Outline each Plasmodium falciparum parasite and classify it by life-cycle stage.
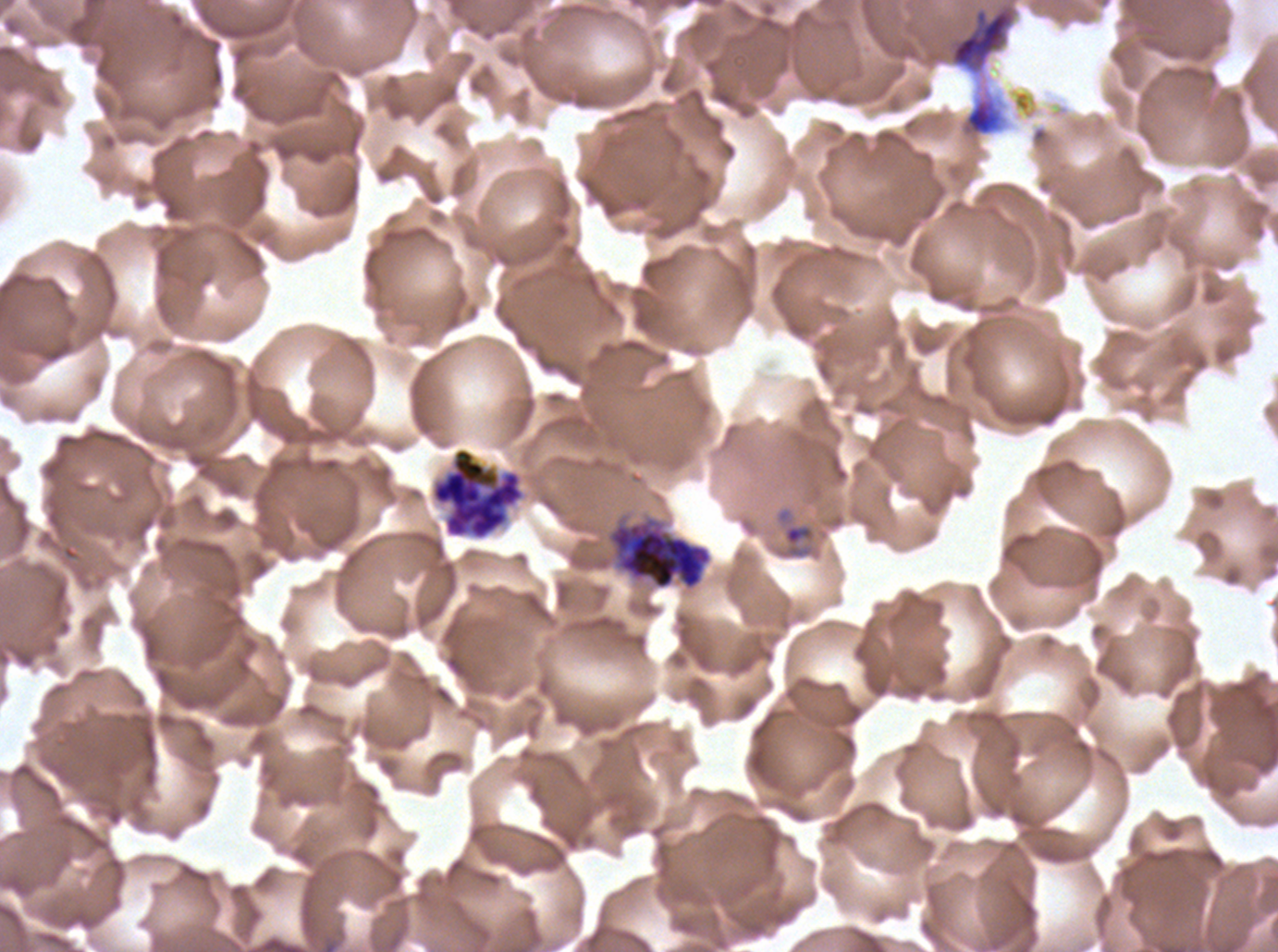
Approximate bounding boxes as [x1, y1, x2, y2] in pixels.
Rings: [775, 507, 817, 560].
Early schizonts: [608, 519, 712, 591].
Segmenters: [429, 446, 527, 542].
No late-ring/early-trophozoite forms, mid trophozoites, late trophozoites, late schizonts, or gametocytes observed.

debris locations = [944, 0, 1019, 76]
life-cycle stages observed = ring, early schizont, segmenter
image size = 1278×952 pixels
field of view = sub-image separated from a larger composite
preparation = thin blood smear
stain = Giemsa
specimen = Plasmodium falciparum from a patient in The Gambia, cultured ex vivo for 24 to 48 hours